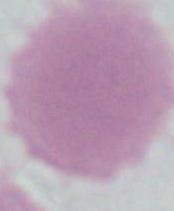

magnification = 1000x
modality = photomicrograph
identification = red blood cell